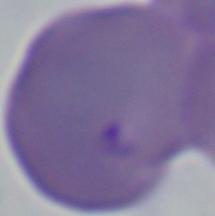

modality = micrograph
magnification = 1000x
identification = Babesia